Classify this cell by malaria status.
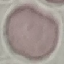
It is uninfected.

preparation: thin blood film
image_type: cell patch, automatically extracted from a larger field of view and resized to 64 × 64 pixels
capture: smartphone through the microscope eyepiece
stain: Giemsa